Evaluate for malaria.
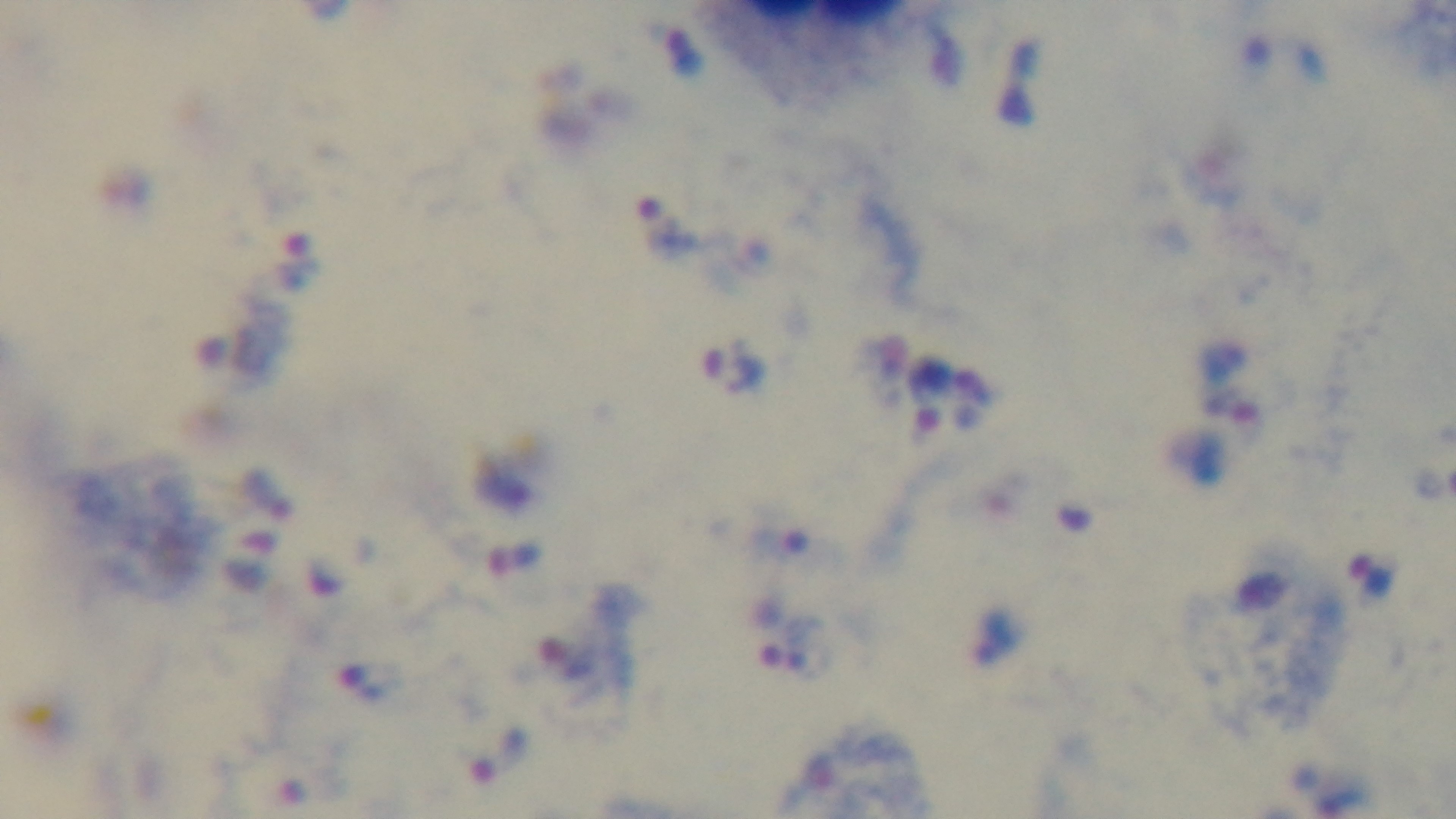
It is infected.

Summary:
  - Preparation: thick smear
  - Objective: 100x oil immersion
  - Stain: Giemsa
  - Modality: light microscopy
  - Field of view: single
  - Capture: mounted 4K digital camera